Identify the preparation type.
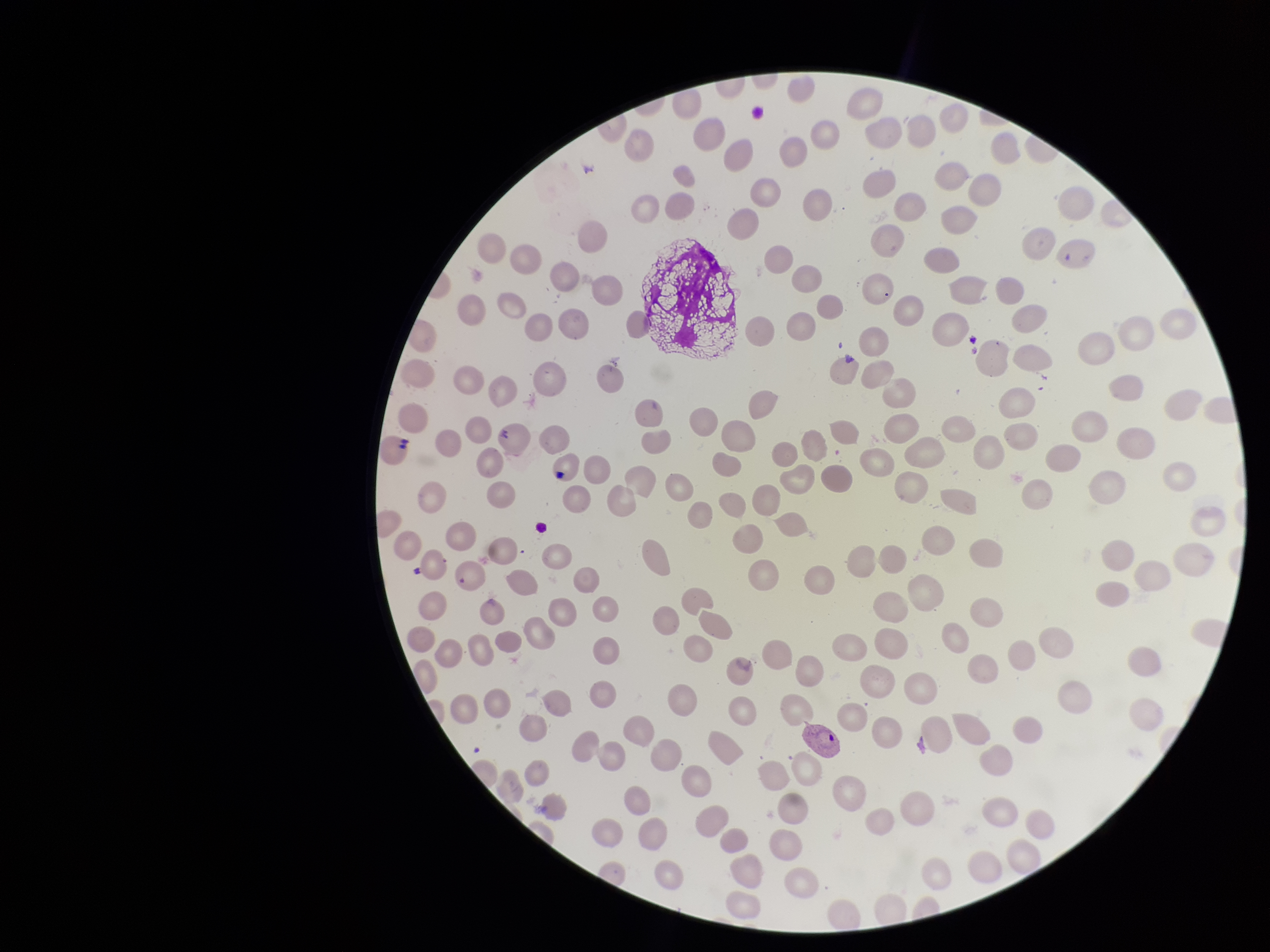
It is a thin blood smear.

Image is 1270×952 pixels. Species reported for this patient: Plasmodium vivax. Photographed through the microscope eyepiece with a smartphone camera. Stained with Giemsa. Patient malaria status: positive. Red blood cell count: 186. One field from this slide. Parasitized red blood cell count: 1. Parasitized red blood cells: seen.